Identify the cell.
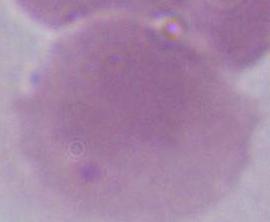

An erythrocyte.

Summary:
  - Magnification: 1000x
  - Modality: micrograph